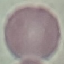

Malaria status: uninfected. Automatically extracted cell patch, resized to 64 × 64 pixels. Thin blood smear. Giemsa-stained preparation. Acquired by smartphone through the microscope eyepiece.